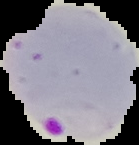
preparation: thin blood smear
image_type: cell region segmented out of the field of view; surrounding area masked to black
image_size: 139×145 pixels
malaria_status: parasitized